Name the blood parasite species.
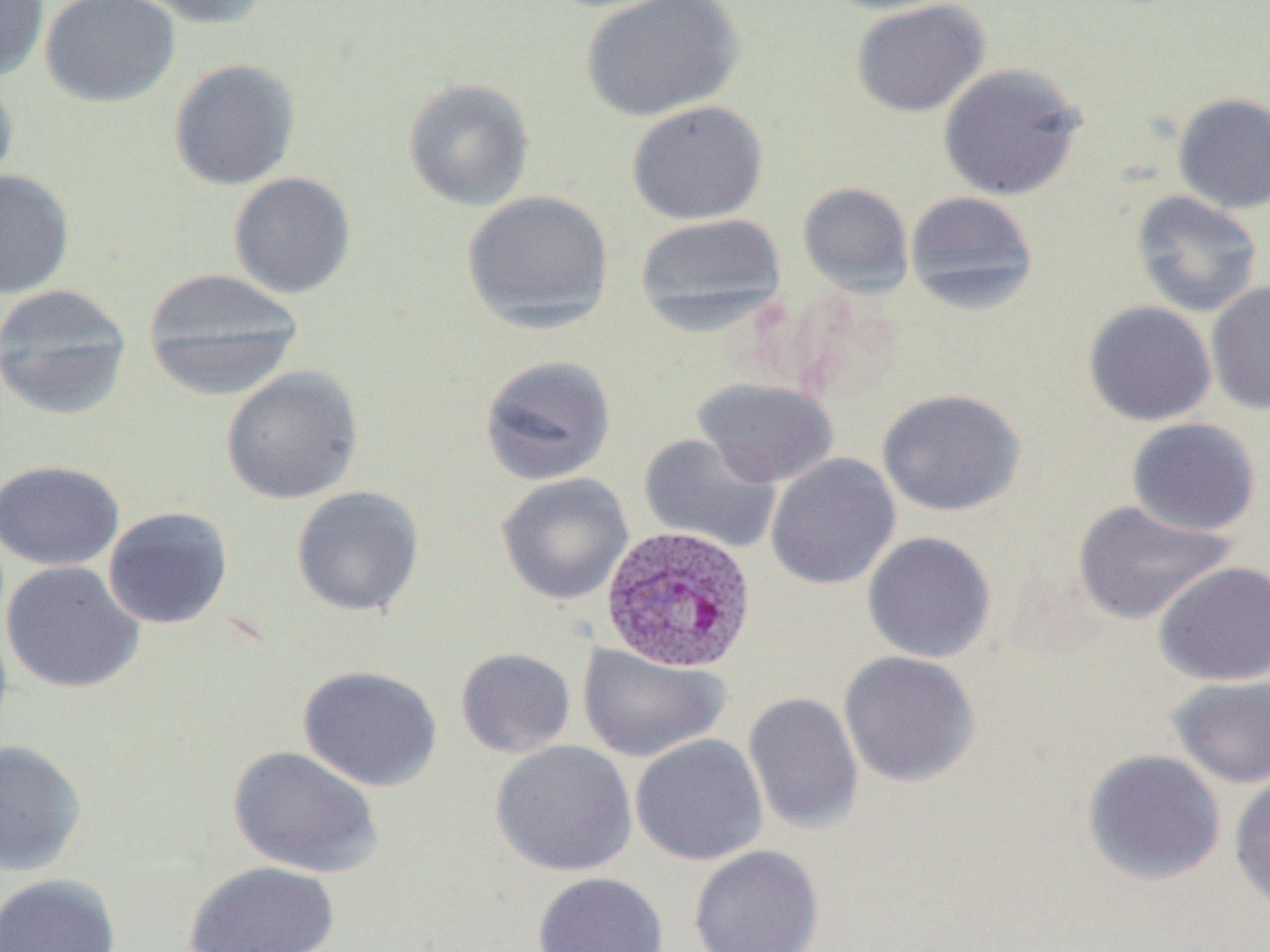

Plasmodium ovale.

uninfected red blood cell locations = approximate bounding boxes as named x1/y1/x2/y2 corners in pixels: (x1=0, y1=0, x2=49, y2=82), (x1=39, y1=0, x2=180, y2=108), (x1=127, y1=0, x2=273, y2=29), (x1=579, y1=0, x2=744, y2=121), (x1=812, y1=0, x2=968, y2=16), (x1=850, y1=0, x2=990, y2=118), (x1=167, y1=58, x2=301, y2=190), (x1=937, y1=63, x2=1085, y2=201), (x1=0, y1=72, x2=19, y2=196), (x1=402, y1=78, x2=535, y2=211), (x1=1171, y1=92, x2=1270, y2=214), (x1=626, y1=100, x2=768, y2=224), (x1=0, y1=167, x2=75, y2=299), (x1=228, y1=171, x2=357, y2=299), (x1=797, y1=181, x2=914, y2=297), (x1=461, y1=190, x2=615, y2=332), (x1=905, y1=190, x2=1038, y2=313), (x1=1130, y1=190, x2=1263, y2=317), (x1=634, y1=212, x2=788, y2=333), (x1=142, y1=267, x2=305, y2=398), (x1=1205, y1=282, x2=1270, y2=414), (x1=0, y1=283, x2=134, y2=420), (x1=1083, y1=301, x2=1217, y2=426), (x1=478, y1=354, x2=617, y2=486), (x1=220, y1=365, x2=364, y2=504), (x1=694, y1=378, x2=839, y2=487), (x1=877, y1=388, x2=1026, y2=516), (x1=1126, y1=417, x2=1261, y2=536), (x1=637, y1=433, x2=782, y2=554), (x1=766, y1=453, x2=900, y2=590), (x1=0, y1=460, x2=125, y2=571), (x1=496, y1=473, x2=634, y2=605), (x1=291, y1=485, x2=425, y2=617), (x1=1071, y1=499, x2=1236, y2=626), (x1=102, y1=506, x2=234, y2=630), (x1=862, y1=531, x2=996, y2=663), (x1=1, y1=560, x2=145, y2=694), (x1=1154, y1=560, x2=1270, y2=686), (x1=578, y1=643, x2=729, y2=763), (x1=455, y1=647, x2=576, y2=758), (x1=838, y1=651, x2=980, y2=787), (x1=298, y1=664, x2=443, y2=792), (x1=1167, y1=675, x2=1270, y2=789), (x1=743, y1=692, x2=864, y2=835), (x1=630, y1=734, x2=768, y2=866), (x1=0, y1=739, x2=87, y2=876), (x1=490, y1=740, x2=637, y2=876), (x1=227, y1=745, x2=383, y2=878), (x1=1082, y1=748, x2=1226, y2=886), (x1=1229, y1=772, x2=1270, y2=915), (x1=688, y1=845, x2=824, y2=952), (x1=182, y1=861, x2=340, y2=952), (x1=533, y1=871, x2=668, y2=952), (x1=0, y1=873, x2=121, y2=952)
preparation = thin blood film
modality = optical microscopy
field of view = single
Plasmodium ovale-infected red blood cell locations = approximate bounding boxes as named x1/y1/x2/y2 corners in pixels: (x1=600, y1=525, x2=758, y2=674)
image size = 1270×952 pixels
stain = May-Grünwald-Giemsa
magnification = 1000x